Identify the parasite.
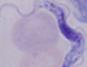
This is a trypanosome.

Summary:
  - Modality: photomicrograph
  - Magnification: 1000x